State the preparation type.
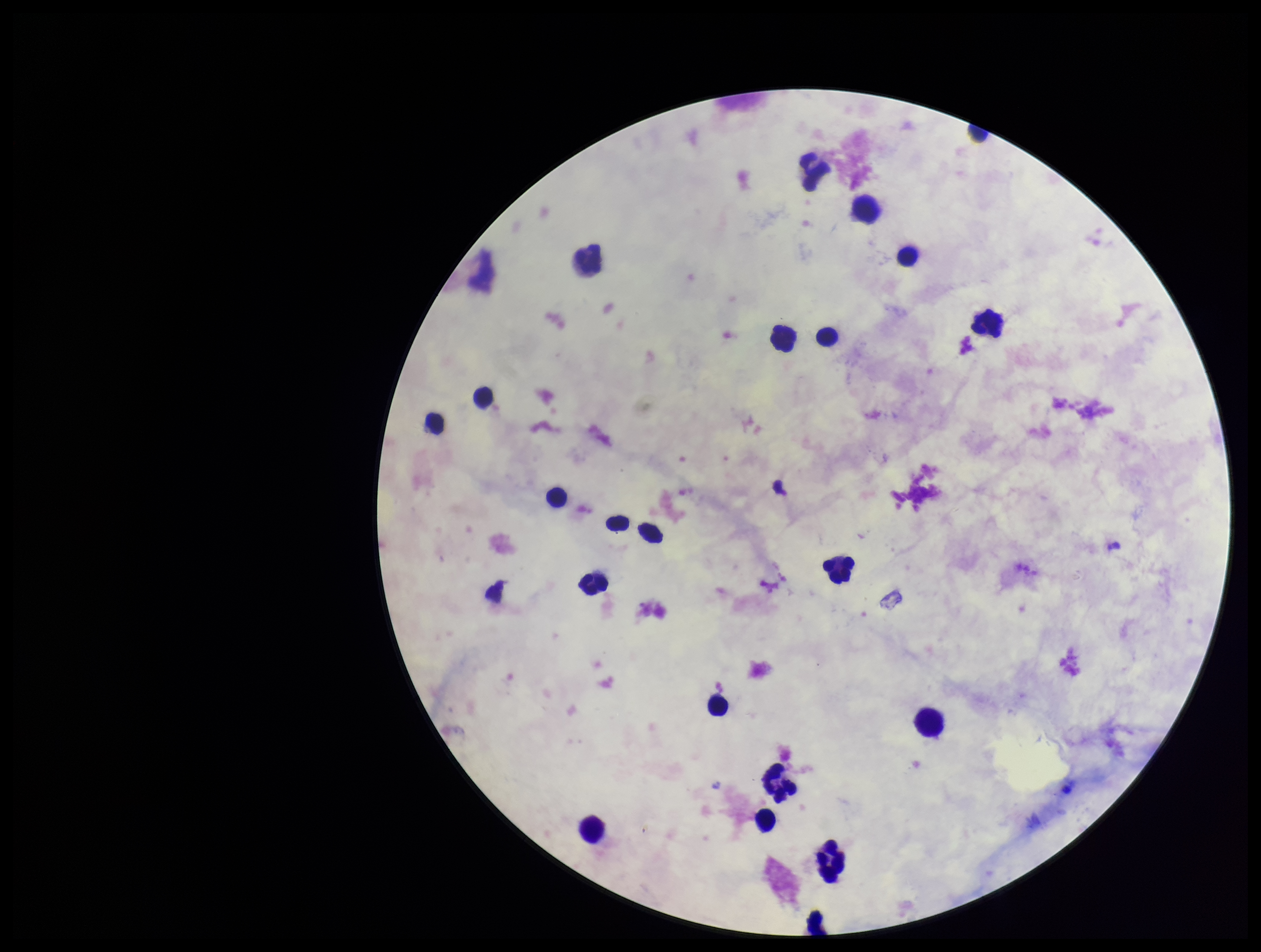

It is a thick blood smear.

Giemsa stain. Parasite count: 0. Patient malaria status: negative. Plasmodium parasites: none identified. Single field of view. Leukocyte count: 22. Image is 1261×952 pixels. Photographed through the microscope eyepiece with a smartphone camera.